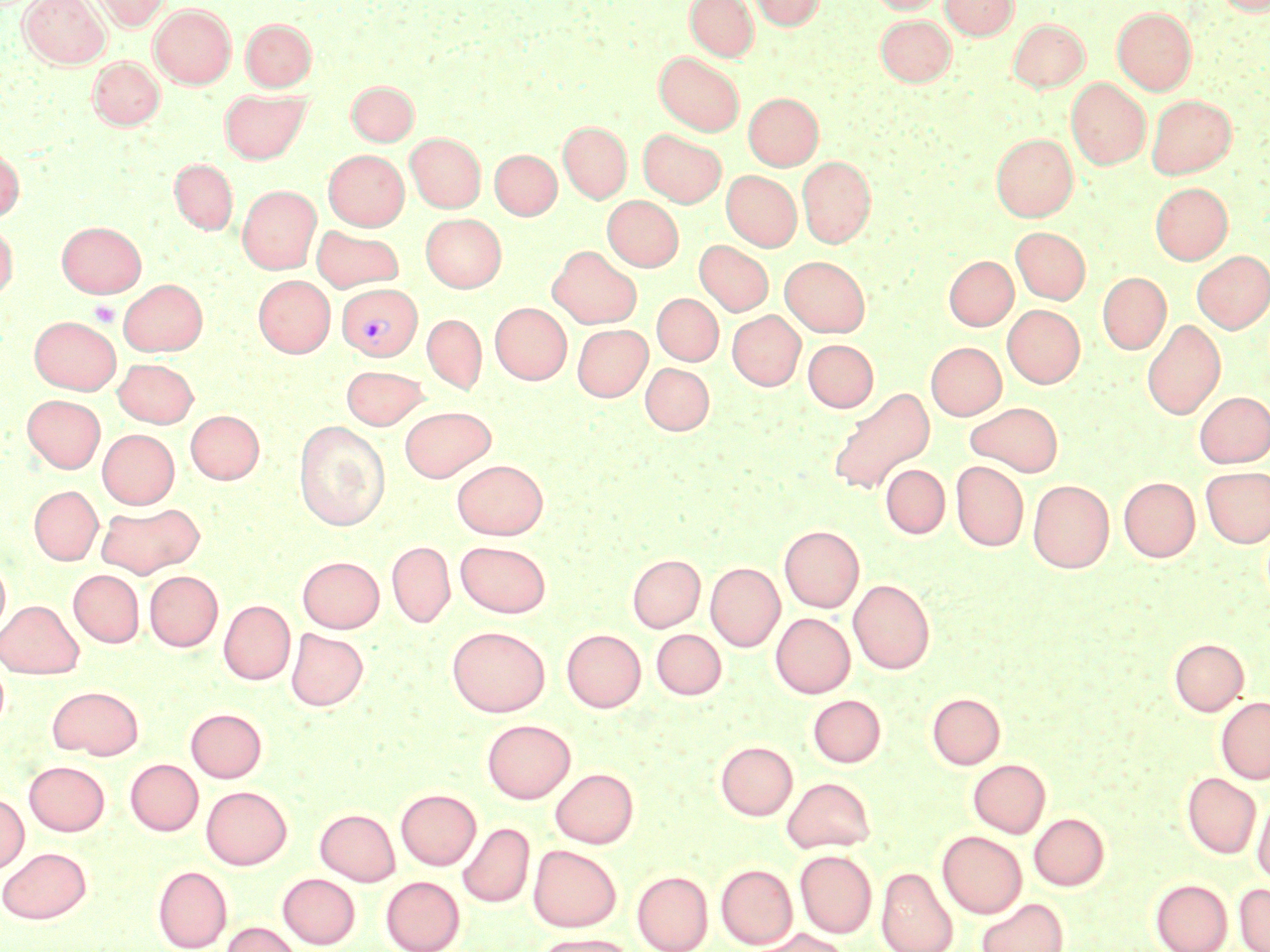

Summary:
  - Coordinate format: approximate bounding boxes as named x1/y1/x2/y2 corners in pixels
  - Uninfected red blood cell locations: (x1=20, y1=0, x2=109, y2=68), (x1=92, y1=0, x2=171, y2=30), (x1=685, y1=0, x2=758, y2=61), (x1=749, y1=0, x2=825, y2=30), (x1=868, y1=0, x2=947, y2=14), (x1=941, y1=0, x2=1017, y2=39), (x1=1215, y1=0, x2=1269, y2=16), (x1=150, y1=4, x2=236, y2=88), (x1=1112, y1=7, x2=1196, y2=94), (x1=876, y1=13, x2=956, y2=86), (x1=241, y1=18, x2=316, y2=91), (x1=1009, y1=18, x2=1089, y2=92), (x1=655, y1=52, x2=744, y2=135), (x1=88, y1=56, x2=164, y2=130), (x1=1066, y1=78, x2=1150, y2=168), (x1=347, y1=81, x2=418, y2=145), (x1=220, y1=89, x2=310, y2=164), (x1=744, y1=93, x2=823, y2=169), (x1=1146, y1=94, x2=1236, y2=178), (x1=558, y1=122, x2=631, y2=202), (x1=638, y1=129, x2=726, y2=207), (x1=405, y1=133, x2=485, y2=212), (x1=991, y1=133, x2=1077, y2=221), (x1=0, y1=144, x2=24, y2=222), (x1=323, y1=150, x2=408, y2=230), (x1=490, y1=150, x2=561, y2=219), (x1=797, y1=156, x2=875, y2=247), (x1=170, y1=159, x2=237, y2=234), (x1=721, y1=170, x2=801, y2=251), (x1=1150, y1=182, x2=1232, y2=264), (x1=238, y1=185, x2=321, y2=273), (x1=602, y1=196, x2=683, y2=271), (x1=421, y1=213, x2=506, y2=292), (x1=0, y1=220, x2=18, y2=300), (x1=57, y1=221, x2=145, y2=296), (x1=311, y1=225, x2=403, y2=291), (x1=1011, y1=227, x2=1090, y2=304), (x1=694, y1=240, x2=774, y2=316), (x1=548, y1=246, x2=641, y2=328), (x1=1192, y1=251, x2=1270, y2=333), (x1=780, y1=256, x2=870, y2=336), (x1=944, y1=256, x2=1018, y2=330), (x1=1098, y1=272, x2=1171, y2=354), (x1=253, y1=275, x2=334, y2=356), (x1=119, y1=278, x2=207, y2=355), (x1=652, y1=293, x2=723, y2=365), (x1=490, y1=302, x2=571, y2=384), (x1=1003, y1=305, x2=1085, y2=388), (x1=727, y1=310, x2=805, y2=390), (x1=422, y1=314, x2=486, y2=394), (x1=29, y1=316, x2=121, y2=394), (x1=1142, y1=319, x2=1226, y2=419), (x1=572, y1=324, x2=651, y2=401), (x1=803, y1=339, x2=878, y2=412), (x1=926, y1=342, x2=1006, y2=420), (x1=113, y1=358, x2=198, y2=427), (x1=640, y1=362, x2=714, y2=434), (x1=341, y1=365, x2=430, y2=430), (x1=827, y1=386, x2=935, y2=493), (x1=1195, y1=391, x2=1270, y2=467), (x1=22, y1=394, x2=105, y2=472), (x1=965, y1=402, x2=1063, y2=476), (x1=399, y1=405, x2=496, y2=482), (x1=186, y1=410, x2=264, y2=484), (x1=294, y1=420, x2=390, y2=530), (x1=97, y1=429, x2=179, y2=508), (x1=452, y1=459, x2=548, y2=539), (x1=951, y1=460, x2=1028, y2=551), (x1=881, y1=464, x2=950, y2=538), (x1=1201, y1=466, x2=1270, y2=547), (x1=1118, y1=476, x2=1200, y2=562), (x1=1028, y1=479, x2=1114, y2=572), (x1=29, y1=486, x2=102, y2=564), (x1=96, y1=502, x2=203, y2=578), (x1=779, y1=525, x2=864, y2=612), (x1=386, y1=541, x2=455, y2=628), (x1=455, y1=541, x2=551, y2=617), (x1=627, y1=554, x2=705, y2=632), (x1=297, y1=556, x2=384, y2=632), (x1=0, y1=557, x2=10, y2=635), (x1=705, y1=562, x2=785, y2=651), (x1=68, y1=569, x2=144, y2=647), (x1=145, y1=571, x2=223, y2=650), (x1=849, y1=579, x2=934, y2=674), (x1=0, y1=600, x2=83, y2=678), (x1=219, y1=600, x2=295, y2=684), (x1=771, y1=613, x2=855, y2=698), (x1=447, y1=625, x2=549, y2=716), (x1=285, y1=628, x2=367, y2=711), (x1=561, y1=629, x2=645, y2=712), (x1=651, y1=629, x2=726, y2=699), (x1=1169, y1=638, x2=1248, y2=716), (x1=47, y1=685, x2=144, y2=759), (x1=927, y1=693, x2=1005, y2=769), (x1=808, y1=694, x2=885, y2=767), (x1=1216, y1=696, x2=1270, y2=783), (x1=186, y1=708, x2=267, y2=782), (x1=481, y1=719, x2=575, y2=803), (x1=716, y1=741, x2=797, y2=819), (x1=125, y1=759, x2=203, y2=835), (x1=968, y1=759, x2=1050, y2=837), (x1=24, y1=761, x2=109, y2=835), (x1=550, y1=768, x2=638, y2=847), (x1=1182, y1=773, x2=1260, y2=858), (x1=782, y1=776, x2=876, y2=853), (x1=201, y1=786, x2=291, y2=869), (x1=396, y1=789, x2=481, y2=870), (x1=1252, y1=793, x2=1270, y2=882), (x1=0, y1=794, x2=28, y2=873), (x1=315, y1=808, x2=400, y2=885), (x1=1030, y1=813, x2=1109, y2=890), (x1=458, y1=822, x2=534, y2=908), (x1=938, y1=831, x2=1027, y2=918), (x1=528, y1=845, x2=621, y2=931), (x1=0, y1=847, x2=91, y2=923), (x1=795, y1=850, x2=876, y2=938), (x1=716, y1=864, x2=797, y2=948), (x1=153, y1=866, x2=232, y2=952), (x1=876, y1=867, x2=957, y2=952), (x1=632, y1=871, x2=713, y2=952), (x1=278, y1=873, x2=360, y2=948), (x1=381, y1=876, x2=465, y2=952), (x1=1151, y1=879, x2=1233, y2=952), (x1=1234, y1=884, x2=1270, y2=952), (x1=976, y1=898, x2=1068, y2=952), (x1=220, y1=922, x2=302, y2=952), (x1=756, y1=928, x2=849, y2=952), (x1=533, y1=933, x2=635, y2=952)
  - Platelet locations: (x1=89, y1=301, x2=119, y2=326)
  - Plasmodium vivax-infected red blood cell locations: (x1=337, y1=283, x2=421, y2=361)
  - Slide-level diagnosis: Plasmodium vivax
  - Preparation: thin blood smear
  - Image size: 1270×952 pixels
  - Magnification: 1000x
  - Stain: May-Grünwald-Giemsa
  - Field of view: single
  - Modality: optical microscopy